Point out each Plasmodium parasite.
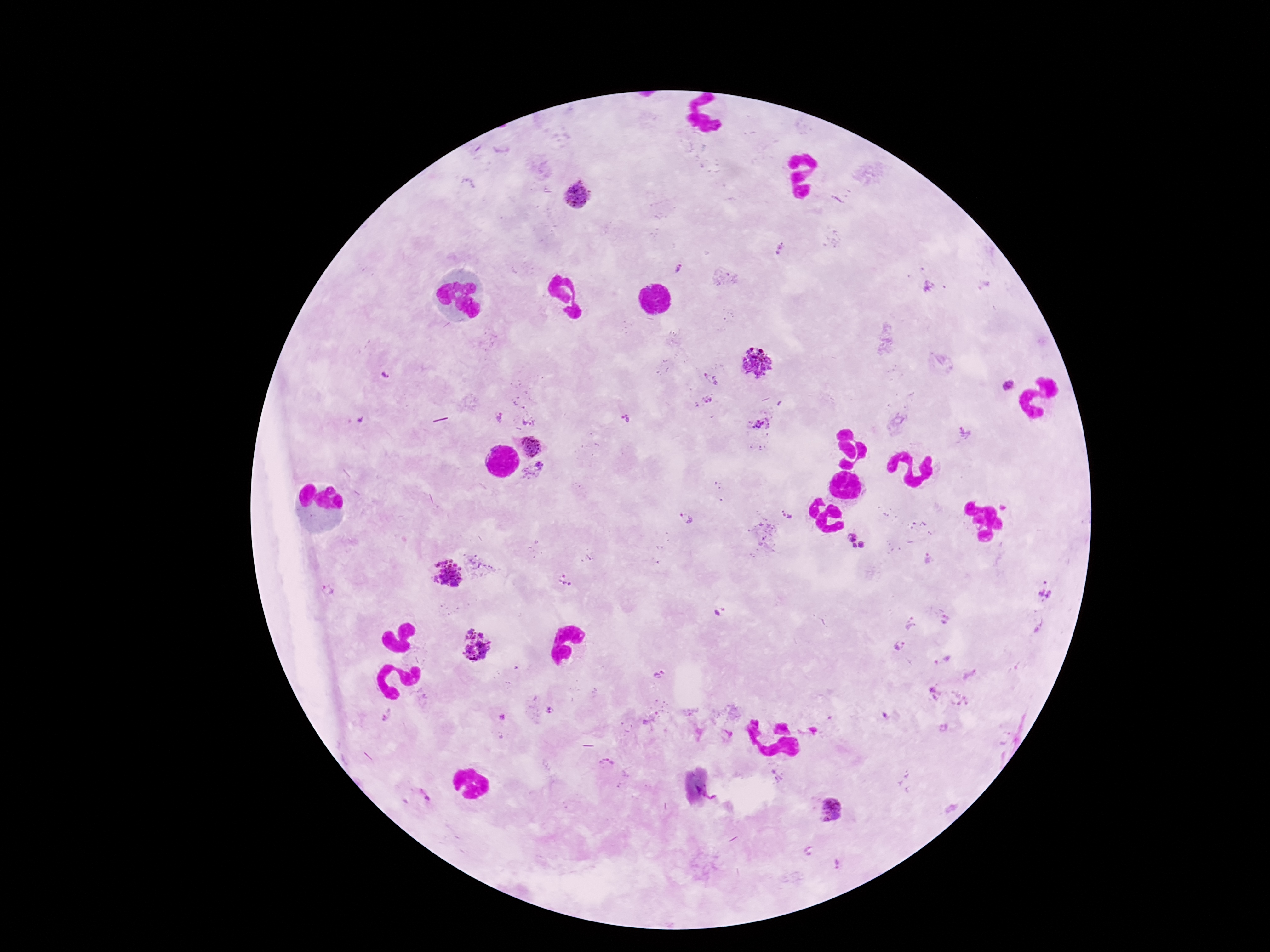
Approximate object centers, in pixels from the top-left corner.
Plasmodium parasites: (x=577, y=196), (x=781, y=250), (x=679, y=266), (x=927, y=286), (x=758, y=361), (x=386, y=377), (x=709, y=380), (x=1008, y=387), (x=707, y=400), (x=500, y=418), (x=626, y=421), (x=528, y=422), (x=760, y=424), (x=530, y=447), (x=535, y=471), (x=787, y=513), (x=687, y=519), (x=858, y=540), (x=929, y=560), (x=450, y=577), (x=565, y=582), (x=1046, y=588), (x=327, y=590), (x=716, y=615), (x=946, y=620), (x=910, y=624), (x=475, y=646), (x=900, y=646), (x=942, y=660), (x=659, y=674), (x=969, y=676), (x=550, y=712), (x=388, y=714), (x=605, y=765), (x=426, y=796), (x=830, y=808), (x=810, y=851), (x=838, y=864).

Image is 1270×952 pixels. Thick blood smear. Smartphone photograph taken through the microscope eyepiece. Patient malaria status: positive. 100x magnification. Giemsa-stained preparation. One field from this slide.